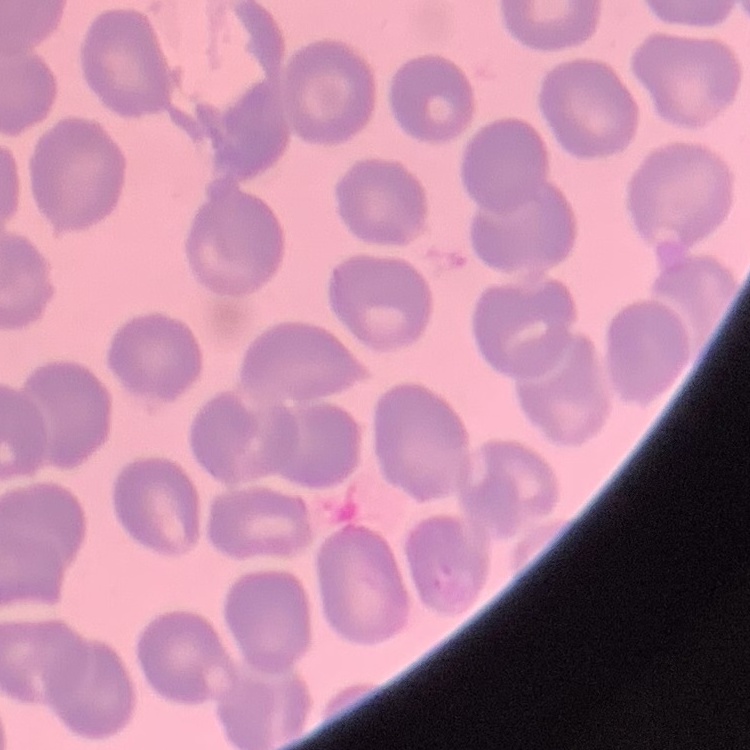

Summary:
  - Erythrocyte morphology: no rouleaux formation
  - Preparation: thin peripheral smear
  - Stain: Field's or Giemsa
  - Image type: one tile cut from a larger photomicrograph